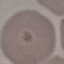

Summary:
  - Malaria status: uninfected
  - Stain: Giemsa
  - Preparation: thin smear
  - Image type: automatically extracted cell patch, resized to 64 × 64 pixels
  - Capture: smartphone camera at the microscope eyepiece